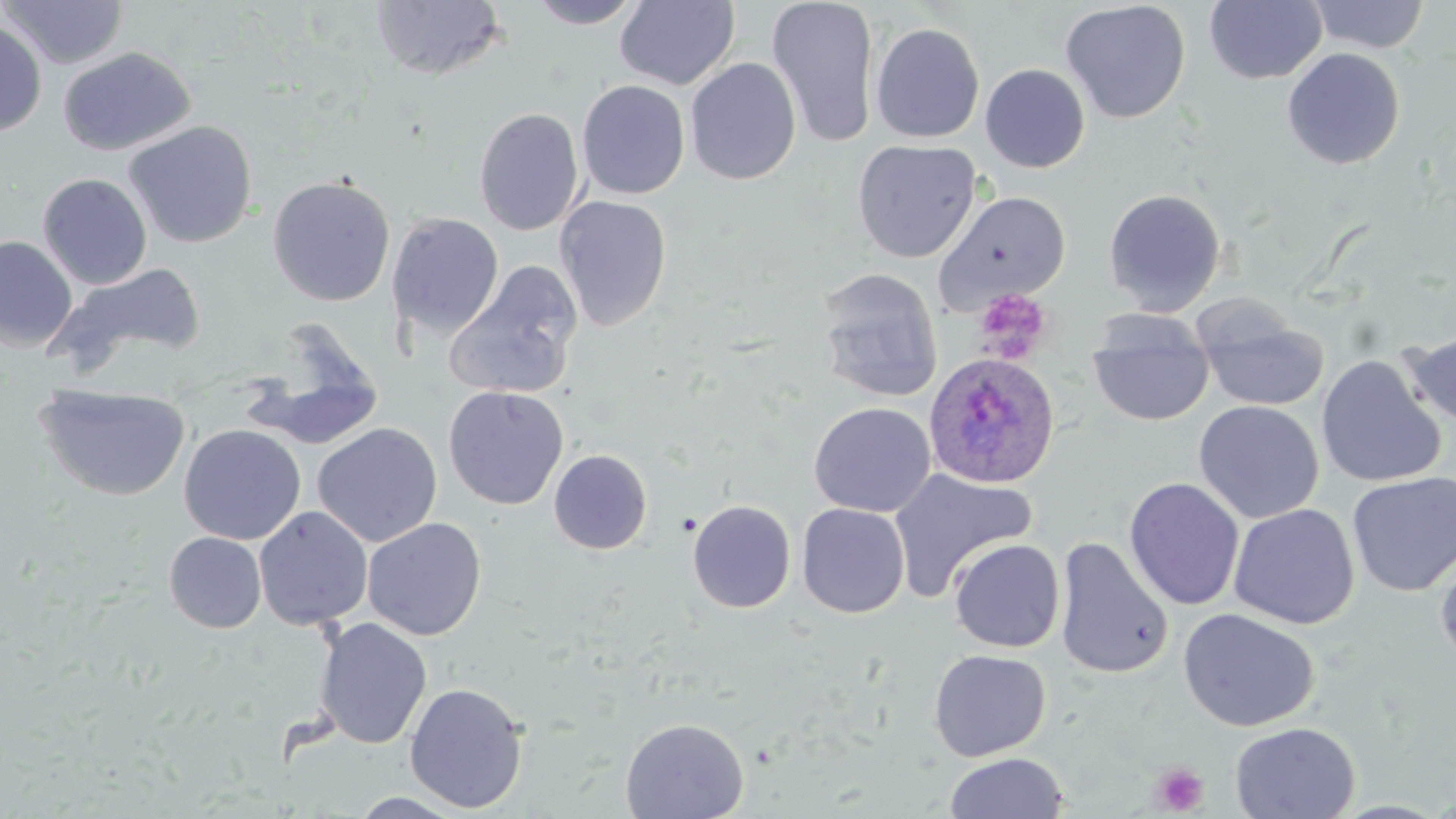
Summary:
  - Coordinate format: approximate bounding boxes as [x1, y1, x2, y2] in pixels
  - Plasmodium ovale-infected red blood cell locations: [924, 352, 1061, 490]
  - Uninfected red blood cell locations: [1, 0, 128, 70], [369, 0, 507, 81], [526, 0, 645, 28], [615, 0, 740, 91], [1307, 0, 1430, 54], [766, 1, 880, 148], [1060, 1, 1191, 123], [1204, 1, 1327, 84], [0, 19, 47, 138], [870, 22, 985, 143], [58, 46, 195, 156], [1282, 47, 1405, 170], [685, 57, 801, 185], [980, 63, 1090, 173], [576, 80, 690, 199], [474, 107, 585, 236], [124, 120, 258, 248], [852, 139, 981, 263], [37, 172, 152, 290], [266, 175, 396, 306], [1103, 188, 1226, 316], [934, 190, 1072, 313], [554, 195, 672, 331], [386, 212, 504, 338], [0, 236, 78, 352], [54, 262, 207, 368], [445, 263, 583, 400], [816, 267, 943, 403], [1193, 298, 1329, 412], [1087, 311, 1214, 427], [239, 327, 386, 453], [1400, 328, 1456, 432], [1316, 355, 1447, 489], [35, 383, 192, 501], [443, 385, 568, 510], [1193, 400, 1324, 523], [809, 401, 935, 518], [312, 422, 443, 547], [178, 424, 306, 545], [548, 449, 653, 554], [888, 468, 1037, 602], [1346, 472, 1456, 597], [1124, 478, 1245, 610], [688, 499, 796, 613], [796, 503, 910, 618], [1228, 503, 1359, 629], [253, 506, 373, 630], [362, 517, 487, 641], [164, 532, 266, 633], [1053, 537, 1174, 679], [949, 538, 1065, 652], [1434, 545, 1456, 669], [1178, 608, 1321, 732], [313, 617, 432, 750], [928, 649, 1051, 762], [404, 681, 529, 813], [620, 717, 749, 819], [1229, 722, 1361, 818], [943, 752, 1069, 819], [349, 791, 469, 818]
  - Platelet locations: [973, 289, 1051, 363], [1150, 762, 1210, 816]
  - Slide-level diagnosis: Plasmodium ovale
  - Modality: light microscopy
  - Image size: 1456×819 pixels
  - Stain: May-Grünwald-Giemsa
  - Field of view: single
  - Magnification: 1000x
  - Preparation: thin blood film